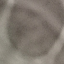

{
  "result": "no malaria parasites seen",
  "image_type": "automatically extracted cell patch, resized to 64 × 64 pixels",
  "preparation": "thin blood film",
  "stain": "Giemsa",
  "capture": "smartphone through the microscope eyepiece"
}